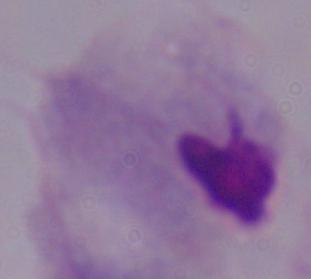 1000x magnification. A trichomonad is seen. Photomicrograph.